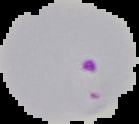
preparation = thin blood film
result = malaria parasites identified
image type = segmented cell region on a black background
image size = 139×124 pixels